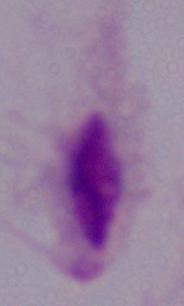

1000x magnification. A trichomonad is seen. Photomicrograph.